Name the blood parasite species.
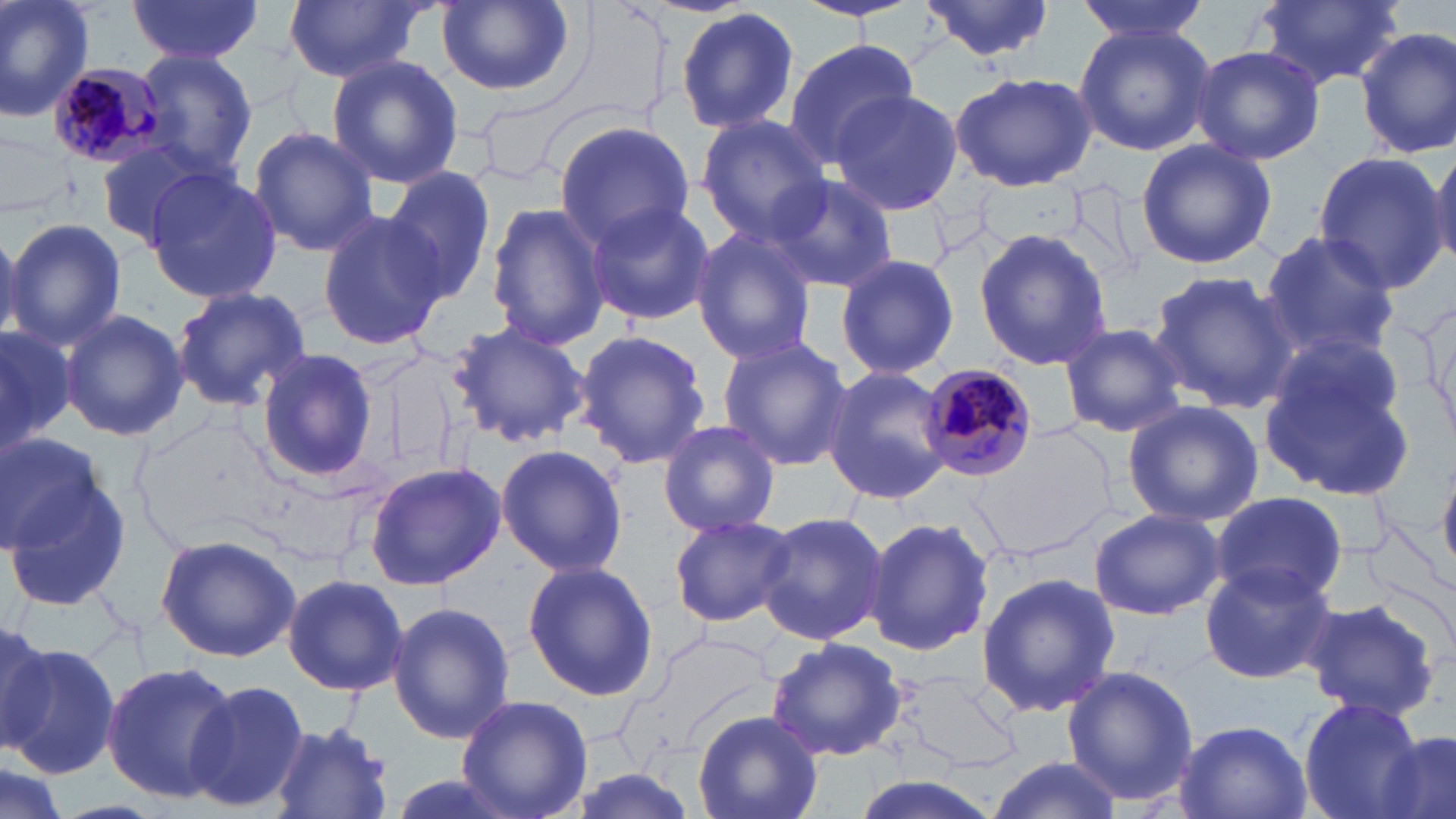

Plasmodium malariae.

field of view = one of a larger specimen
Plasmodium malariae-infected red blood cell locations = approximate bounding boxes as (x1,y1)-(x2,y2) corner pairs in pixels: (47,62)-(171,169), (919,363)-(1041,481)
modality = light microscopy
image size = 1456×819 pixels
stain = May-Grünwald-Giemsa
magnification = 1000x
uninfected red blood cell locations = approximate bounding boxes as (x1,y1)-(x2,y2) corner pairs in pixels: (0,0)-(95,124), (125,0)-(264,62), (282,0)-(430,83), (1077,0)-(1209,45), (1249,0)-(1407,90), (434,1)-(578,97), (919,1)-(1056,61), (675,7)-(800,136), (1074,23)-(1216,157), (1356,27)-(1456,161), (783,38)-(919,167), (1192,45)-(1326,166), (135,51)-(258,182), (327,55)-(463,189), (950,71)-(1098,192), (832,89)-(963,217), (696,113)-(833,244), (553,120)-(695,248), (249,125)-(378,257), (96,138)-(221,246), (1135,139)-(1277,270), (1426,149)-(1456,271), (1312,151)-(1448,291), (143,166)-(282,307), (383,166)-(500,305), (761,173)-(898,293), (486,201)-(612,351), (584,202)-(713,325), (316,211)-(448,352), (4,217)-(126,351), (691,227)-(820,365), (974,227)-(1111,372), (1259,230)-(1402,357), (834,252)-(959,383), (1147,269)-(1296,413), (171,286)-(313,411), (60,309)-(188,442), (448,320)-(590,448), (1056,322)-(1188,439), (0,323)-(74,455), (572,329)-(710,469), (1259,335)-(1420,502), (716,337)-(853,471), (255,349)-(379,486), (823,367)-(953,505), (1121,399)-(1264,528), (657,417)-(781,535), (980,426)-(1118,557), (0,431)-(101,549), (495,444)-(628,578), (366,460)-(506,589), (1439,462)-(1456,584), (5,474)-(133,614), (1210,489)-(1348,607), (1089,508)-(1224,620), (757,510)-(888,647), (667,512)-(796,629), (865,515)-(993,657), (156,532)-(300,662), (521,559)-(660,704), (1198,561)-(1337,684), (976,570)-(1121,720), (282,572)-(408,695), (1301,596)-(1443,720), (387,601)-(514,744), (0,615)-(51,752), (765,636)-(909,761), (5,641)-(119,775), (102,662)-(238,801), (1059,666)-(1199,808), (898,671)-(1024,775), (184,678)-(309,815), (458,694)-(593,819), (1297,697)-(1426,819), (692,710)-(822,819), (1173,719)-(1314,819), (268,722)-(396,819), (1376,727)-(1456,819), (984,755)-(1119,819)
preparation = thin blood smear